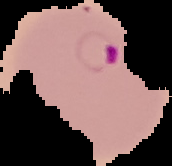

Summary:
  - Preparation: thin blood smear
  - Image type: cell region segmented out of the field of view; surrounding area masked to black
  - Image size: 172×166 pixels
  - Result: malaria parasites identified